Locate and identify every blood parasite.
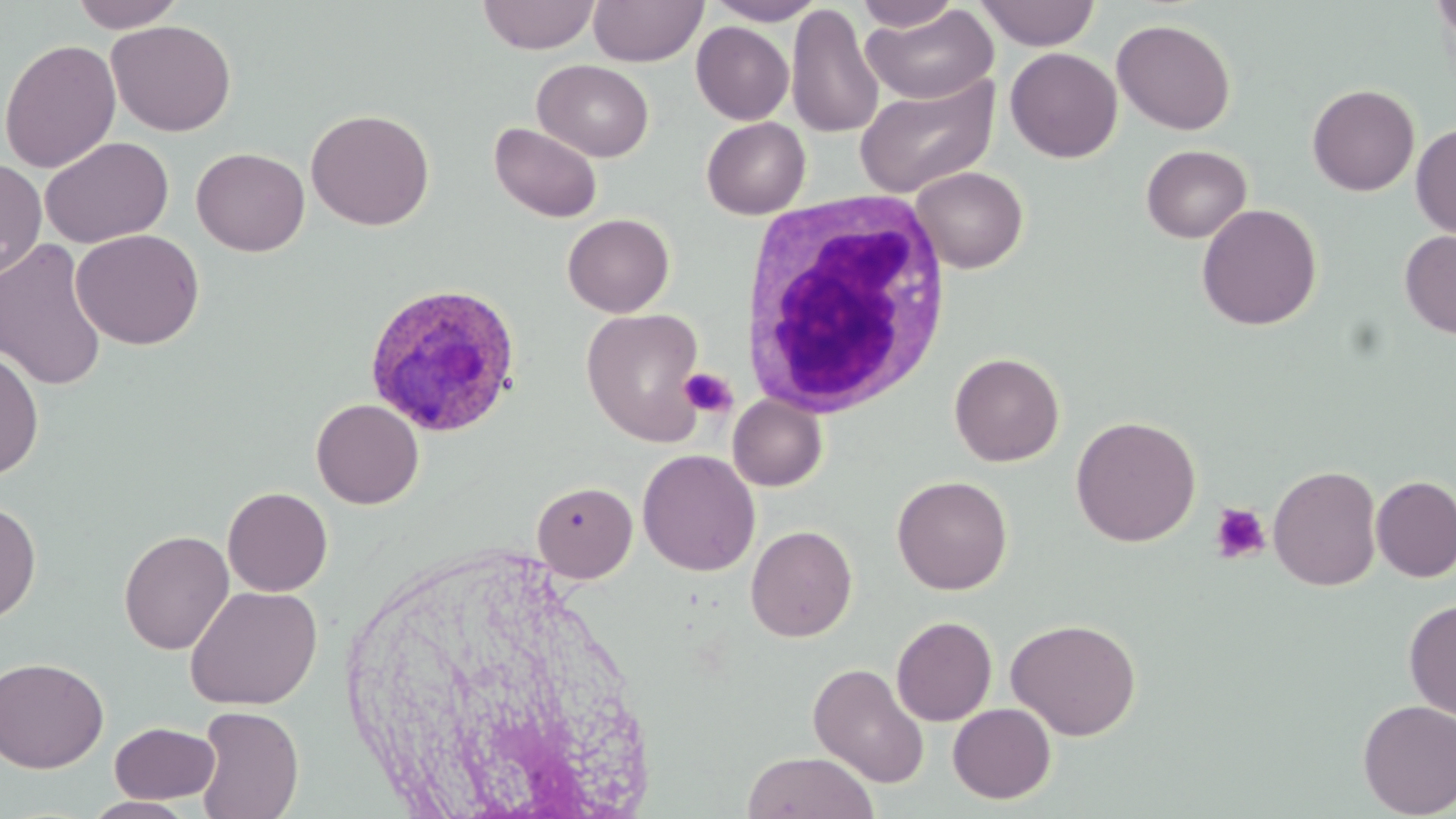

Approximate bounding boxes as (x1,y1)-(x2,y2) corner pairs in pixels.
Plasmodium ovale-infected red blood cells: (363,281)-(525,440).
No Plasmodium falciparum, Plasmodium malariae, Plasmodium vivax, Babesia divergens, or Trypanosoma brucei observed.

slide-level diagnosis = Plasmodium ovale
white blood cell locations = approximate bounding boxes as (x1,y1)-(x2,y2) corner pairs in pixels: (736,190)-(955,419)
platelet locations = approximate bounding boxes as (x1,y1)-(x2,y2) corner pairs in pixels: (678,368)-(737,417), (1210,503)-(1271,564)
magnification = 1000x
preparation = thin blood smear
image size = 1456×819 pixels
modality = light microscopy
uninfected red blood cell locations = approximate bounding boxes as (x1,y1)-(x2,y2) corner pairs in pixels: (68,0)-(186,32), (477,0)-(600,54), (588,0)-(708,66), (706,0)-(825,25), (854,0)-(963,31), (975,0)-(1099,50), (785,4)-(884,139), (862,4)-(997,105), (1112,18)-(1236,135), (106,19)-(236,137), (691,21)-(794,124), (0,38)-(121,173), (1005,47)-(1122,163), (533,60)-(654,162), (853,74)-(998,199), (1307,83)-(1420,196), (306,108)-(435,230), (702,117)-(811,219), (489,122)-(603,223), (1411,123)-(1456,239), (40,136)-(174,248), (1140,144)-(1251,243), (191,147)-(310,256), (0,158)-(46,281), (911,166)-(1028,273), (1196,203)-(1322,331), (562,213)-(674,317), (70,228)-(205,350), (1399,229)-(1456,339), (1,238)-(109,391), (581,308)-(708,446), (0,347)-(44,481), (949,352)-(1064,466), (727,394)-(828,491), (311,398)-(424,509), (1070,415)-(1201,547), (637,449)-(760,576), (1268,464)-(1382,591), (891,475)-(1013,595), (1371,475)-(1456,582), (532,480)-(637,582), (222,487)-(333,597), (0,499)-(42,624), (745,524)-(858,642), (118,529)-(234,654), (185,585)-(322,709), (1403,598)-(1456,722), (891,616)-(997,726), (1005,617)-(1142,740), (0,656)-(109,773), (808,661)-(930,789), (1356,699)-(1456,817), (947,702)-(1056,804), (193,705)-(304,819), (110,722)-(220,803), (742,750)-(879,819), (81,796)-(199,818)
field of view = single
stain = May-Grünwald-Giemsa